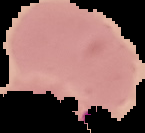
image_type: segmented cell region on a black background
preparation: thin blood film
malaria_status: parasitized
image_size: 145×133 pixels